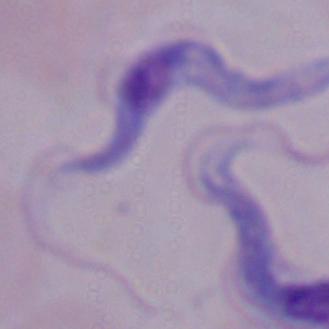
Summary:
  - Magnification: 1000x
  - Modality: photomicrograph
  - Identification: trypanosome